Locate every Plasmodium parasite.
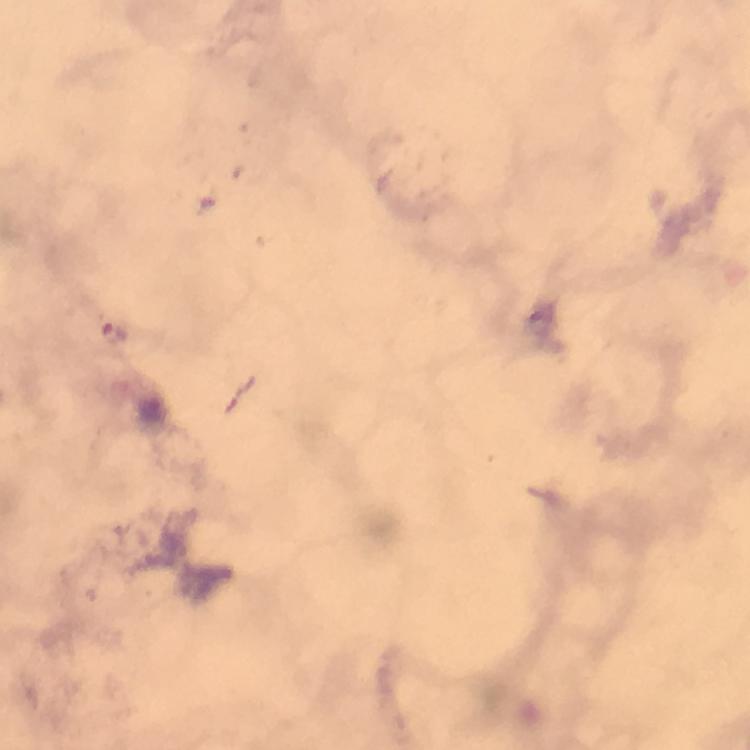

Approximate object centers, in pixels from the top-left corner.
Plasmodium parasites: (x=114, y=331).

immersion oil = used
preparation = thick blood smear
image size = 750×750 pixels
cropped from = one field of view
capture = smartphone mounted on the microscope
context = from a diagnostic examination for malaria
stain = Giemsa
magnification = 100x